Classify this cell by malaria status.
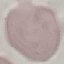
Uninfected.

{
  "preparation": "thin smear",
  "image_type": "automatically extracted cell patch, resized to 64 × 64 pixels",
  "stain": "Giemsa",
  "capture": "smartphone camera at the microscope eyepiece"
}